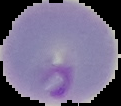

Summary:
  - Image type: cell region segmented out of the field of view; surrounding area masked to black
  - Preparation: thin blood smear
  - Image size: 121×106 pixels
  - Result: Plasmodium parasites detected